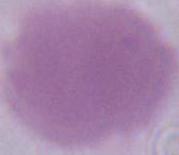
Summary:
  - Identification: red blood cell
  - Magnification: 1000x
  - Modality: micrograph